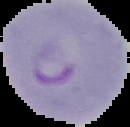
From a thin blood smear. Image is 130×127 pixels. Cell region segmented out of the field of view; the surrounding area is masked to black. Malaria status: parasitized.